Name the blood parasite species.
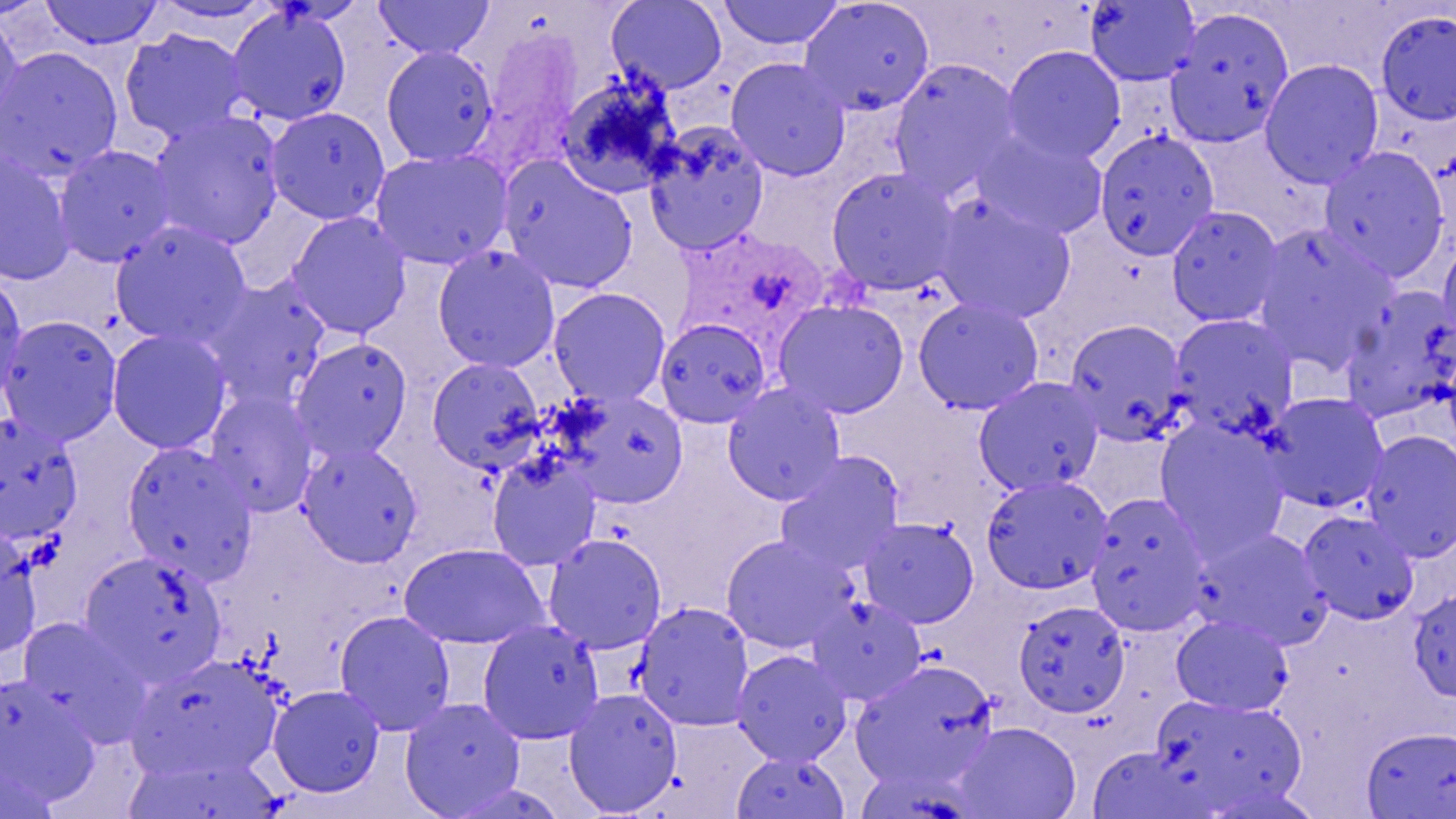

Plasmodium ovale.

image size = 1456×819 pixels
stain = May-Grünwald-Giemsa
field of view = single
uninfected red blood cell locations = approximate bounding boxes as (x1,y1)-(x2,y2) corner pairs in pixels: (39,0)-(164,49), (374,0)-(495,59), (606,0)-(728,94), (717,0)-(846,51), (799,0)-(935,116), (147,1)-(279,26), (1084,1)-(1201,86), (226,5)-(352,126), (1166,7)-(1294,147), (1376,11)-(1456,124), (0,13)-(24,138), (120,28)-(249,144), (1002,45)-(1126,164), (381,46)-(498,165), (0,47)-(122,179), (726,58)-(851,181), (888,60)-(1022,200), (1260,60)-(1384,188), (556,74)-(682,199), (266,106)-(390,225), (149,111)-(285,249), (644,123)-(770,255), (974,131)-(1108,240), (1094,131)-(1219,259), (54,145)-(176,266), (1318,146)-(1450,282), (370,148)-(513,270), (0,151)-(76,286), (497,156)-(638,294), (825,167)-(961,295), (933,195)-(1075,324), (1166,206)-(1283,327), (287,211)-(411,338), (110,221)-(251,348), (1253,224)-(1397,370), (1437,235)-(1456,353), (431,246)-(561,372), (0,275)-(27,405), (202,276)-(332,410), (1338,286)-(1456,424), (548,287)-(671,407), (913,297)-(1044,414), (772,299)-(910,417), (0,315)-(122,446), (1169,315)-(1298,438), (655,318)-(772,427), (1065,319)-(1188,444), (107,329)-(231,454), (290,338)-(412,461), (427,357)-(546,473), (974,377)-(1104,495), (722,384)-(846,506), (205,390)-(318,517), (562,391)-(689,508), (1262,392)-(1390,513), (0,413)-(83,545), (1154,419)-(1289,556), (1360,429)-(1456,562), (297,441)-(423,568), (121,442)-(258,583), (486,452)-(602,570), (774,452)-(906,575), (981,475)-(1112,594), (1085,493)-(1211,636), (1299,510)-(1419,625), (859,518)-(979,628), (1196,528)-(1334,652), (0,530)-(41,658), (543,534)-(667,653), (720,534)-(856,654), (399,543)-(549,649), (80,551)-(226,685), (1408,589)-(1456,701), (808,597)-(926,705), (1014,601)-(1130,718), (633,602)-(754,730), (334,610)-(455,736), (1171,615)-(1292,716), (18,618)-(149,743), (478,621)-(604,743), (732,650)-(852,765), (126,654)-(284,782), (850,659)-(999,793), (0,675)-(99,801), (268,685)-(385,797), (564,688)-(682,815), (1151,694)-(1308,813), (399,698)-(526,818), (953,722)-(1082,818), (1360,726)-(1456,818), (1088,747)-(1212,818), (732,751)-(849,818), (124,753)-(281,819), (1,756)-(60,819), (444,782)-(568,819), (1200,784)-(1322,819)
modality = optical microscopy
Plasmodium ovale-infected red blood cell locations = approximate bounding boxes as (x1,y1)-(x2,y2) corner pairs in pixels: (469,30)-(591,178), (676,226)-(842,340)
magnification = 1000x
preparation = thin blood film
platelet locations = approximate bounding boxes as (x1,y1)-(x2,y2) corner pairs in pixels: (20,533)-(66,571)